State which parasite is depicted.
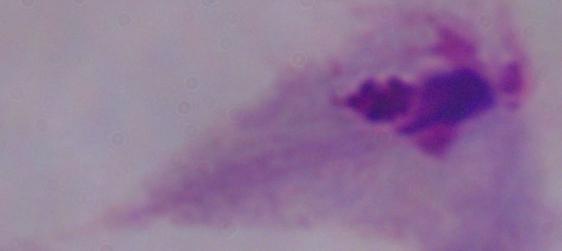

A trichomonad.

modality = photomicrograph
magnification = 1000x